Report the malaria status of this cell.
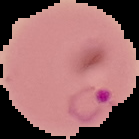

Parasitized.

{
  "image_type": "segmented cell region on a black background",
  "preparation": "thin blood smear",
  "image_size": "139×139 pixels"
}